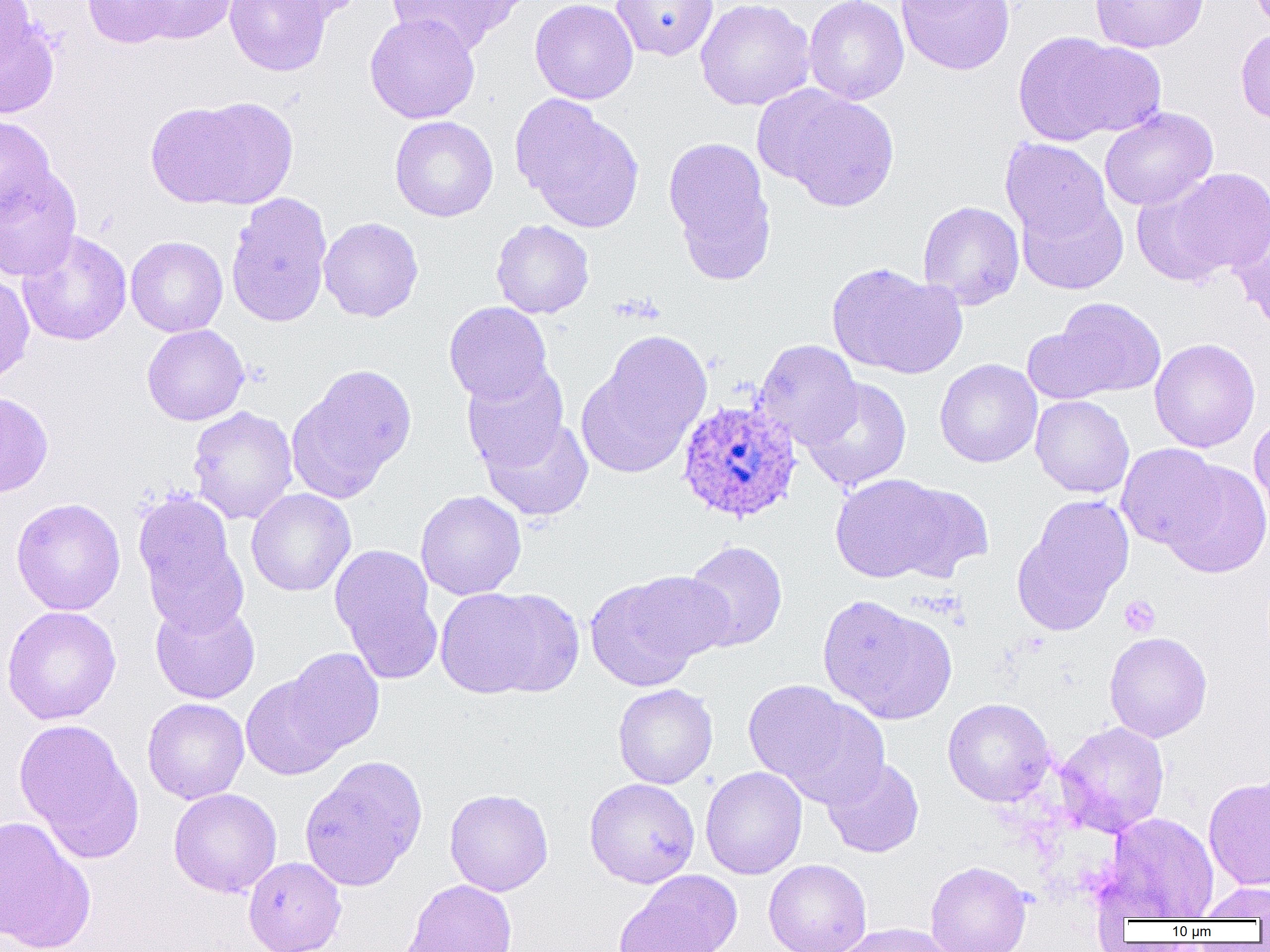

slide-level diagnosis = Plasmodium ovale
modality = light microscopy
image size = 1270×952 pixels
Plasmodium ovale-infected red blood cell locations = approximate bounding boxes as (x1, y1, x2, y2) in pixels: (676, 397, 803, 524)
preparation = thin blood smear
magnification = 1000x
platelet locations = approximate bounding boxes as (x1, y1, x2, y2) in pixels: (1119, 596, 1160, 637)
uninfected red blood cell locations = approximate bounding boxes as (x1, y1, x2, y2) in pixels: (0, 0, 35, 70), (82, 0, 179, 49), (133, 0, 238, 44), (224, 0, 332, 77), (261, 0, 368, 23), (385, 0, 526, 54), (529, 0, 638, 104), (611, 0, 718, 61), (694, 0, 815, 111), (803, 0, 909, 105), (895, 0, 1015, 76), (1090, 0, 1209, 53), (1083, 4, 1194, 97), (0, 9, 60, 120), (364, 12, 480, 124), (1235, 28, 1270, 126), (1013, 31, 1133, 146), (1061, 40, 1167, 137), (758, 85, 899, 211), (146, 96, 297, 210), (513, 96, 646, 233), (1100, 107, 1218, 211), (0, 114, 58, 220), (389, 116, 498, 222), (664, 136, 777, 281), (1000, 138, 1113, 245), (0, 166, 82, 281), (1164, 167, 1270, 277), (1131, 183, 1231, 287), (1015, 188, 1128, 295), (226, 191, 333, 328), (918, 200, 1025, 310), (1229, 214, 1270, 332), (318, 217, 424, 322), (490, 219, 595, 319), (17, 229, 133, 346), (126, 236, 228, 337), (827, 262, 966, 380), (0, 272, 34, 387), (1047, 297, 1166, 399), (444, 302, 553, 406), (141, 324, 250, 426), (1022, 324, 1117, 405), (580, 331, 712, 476), (1149, 338, 1260, 453), (755, 340, 863, 449), (934, 359, 1042, 468), (288, 363, 417, 501), (462, 363, 571, 475), (802, 377, 912, 491), (0, 391, 53, 499), (1030, 395, 1134, 498), (187, 406, 299, 525), (478, 414, 594, 522), (1248, 415, 1270, 527), (1116, 442, 1224, 551), (1161, 460, 1270, 579), (830, 473, 956, 583), (888, 482, 994, 582), (246, 488, 356, 597), (415, 490, 527, 600), (1014, 495, 1134, 635), (134, 496, 246, 631), (11, 498, 126, 616), (681, 540, 787, 653), (329, 544, 442, 684), (584, 573, 721, 690), (434, 586, 567, 699), (818, 595, 956, 725), (150, 598, 260, 704), (1, 605, 121, 725), (1104, 631, 1212, 742), (283, 648, 385, 757), (241, 674, 346, 780), (743, 679, 885, 803), (613, 683, 718, 789), (142, 698, 249, 804), (943, 698, 1055, 807), (13, 718, 144, 863), (1054, 721, 1170, 837), (299, 755, 428, 891), (821, 756, 924, 858), (700, 766, 807, 880), (1203, 775, 1270, 891), (584, 778, 700, 888), (168, 788, 282, 898), (444, 788, 553, 896), (1104, 812, 1219, 920), (0, 815, 96, 952), (243, 857, 346, 952), (763, 859, 872, 952), (925, 860, 1031, 952), (617, 870, 741, 952), (402, 878, 518, 952), (1195, 882, 1270, 920), (833, 922, 957, 952)
field of view = single